Locate every blood parasite and identify its species.
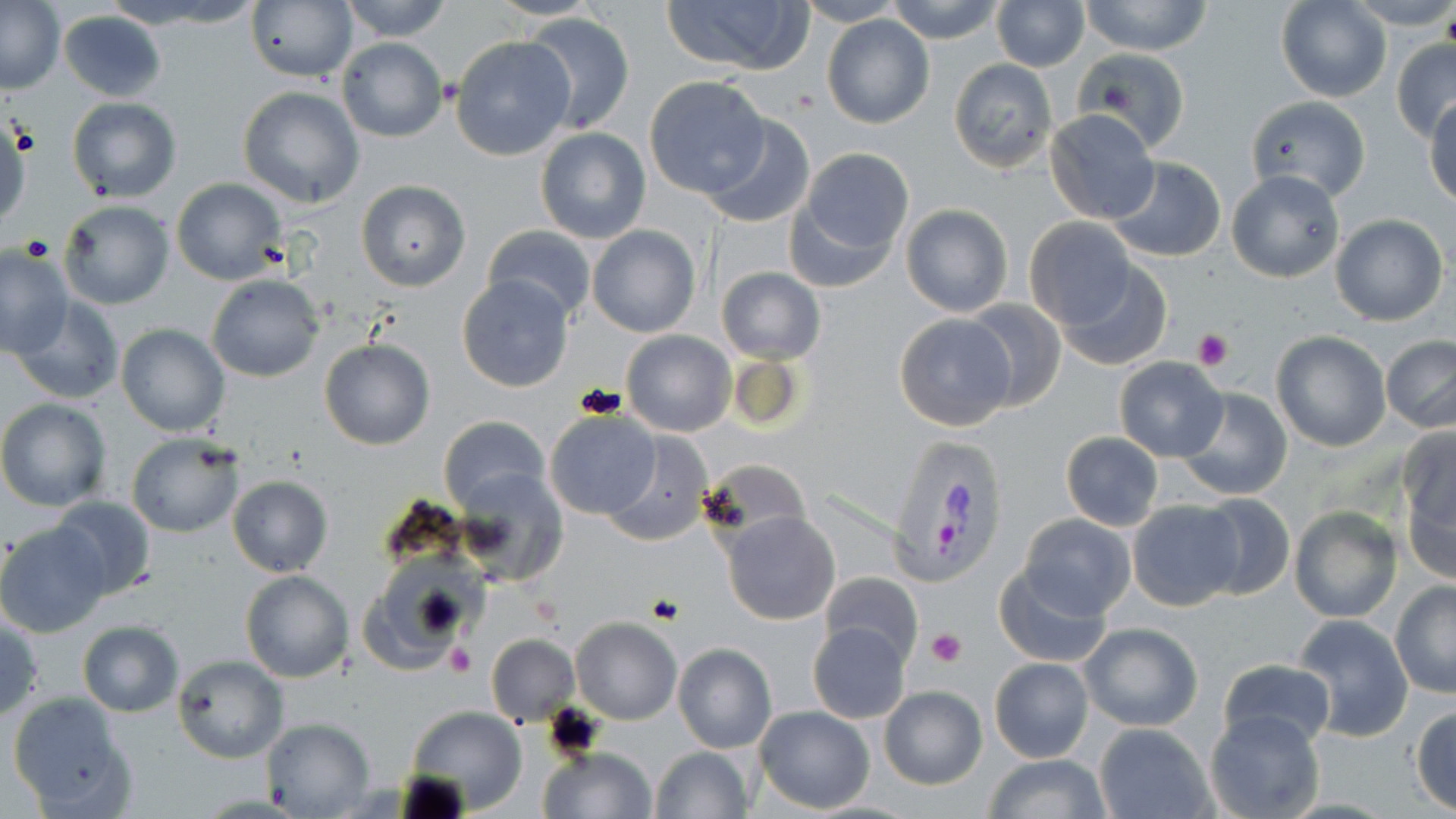

Approximate bounding boxes as [x1, y1, x2, y2] in pixels.
Plasmodium vivax-infected red blood cells: [884, 433, 1009, 587].
No Plasmodium falciparum, Plasmodium ovale, Plasmodium malariae, Babesia divergens, or Trypanosoma brucei observed.

Summary:
  - Platelet locations: [1194, 330, 1234, 368], [927, 628, 967, 668], [444, 641, 475, 675]
  - Uninfected red blood cell locations: [102, 0, 250, 30], [338, 0, 454, 41], [660, 0, 813, 77], [794, 0, 906, 27], [885, 0, 1006, 44], [992, 0, 1088, 71], [1079, 0, 1215, 55], [1347, 0, 1456, 31], [1, 1, 64, 94], [1274, 1, 1392, 103], [246, 2, 356, 82], [59, 10, 167, 104], [521, 11, 635, 135], [822, 14, 935, 129], [450, 35, 576, 161], [335, 36, 447, 143], [1391, 37, 1456, 141], [1072, 48, 1189, 152], [949, 58, 1058, 173], [643, 75, 768, 196], [236, 86, 365, 208], [1245, 96, 1371, 204], [66, 97, 182, 202], [1425, 101, 1456, 207], [1043, 109, 1160, 225], [0, 112, 32, 233], [698, 115, 816, 229], [535, 126, 650, 242], [790, 149, 914, 274], [1106, 156, 1227, 263], [1227, 169, 1343, 282], [171, 177, 288, 285], [356, 180, 471, 291], [61, 191, 287, 298], [59, 199, 175, 310], [899, 204, 1014, 317], [1330, 213, 1448, 326], [1024, 217, 1136, 326], [587, 224, 700, 339], [482, 225, 597, 322], [0, 245, 74, 358], [1057, 259, 1172, 371], [717, 267, 824, 363], [456, 273, 575, 392], [207, 274, 324, 382], [11, 295, 126, 406], [964, 299, 1065, 412], [892, 312, 1019, 432], [116, 324, 230, 437], [621, 329, 736, 436], [1271, 331, 1391, 452], [1380, 335, 1456, 433], [319, 338, 434, 450], [1113, 356, 1228, 461], [1174, 387, 1294, 501], [0, 399, 113, 511], [544, 410, 659, 520], [439, 416, 550, 512], [1396, 427, 1456, 551], [603, 432, 713, 547], [1060, 432, 1164, 530], [126, 433, 246, 538], [697, 459, 808, 542], [458, 467, 569, 588], [227, 474, 332, 577], [1193, 493, 1294, 601], [48, 495, 157, 600], [1126, 499, 1242, 611], [1289, 505, 1401, 623], [721, 512, 840, 626], [1018, 512, 1137, 620], [0, 521, 110, 636], [365, 557, 477, 669], [992, 565, 1114, 668], [241, 570, 353, 683], [819, 572, 923, 671], [1390, 580, 1456, 698], [1292, 614, 1414, 741], [1, 615, 43, 722], [571, 617, 682, 724], [76, 620, 184, 716], [808, 622, 911, 723], [1079, 622, 1203, 732], [570, 629, 777, 737], [485, 635, 579, 726], [672, 643, 777, 753], [172, 654, 287, 762], [989, 658, 1094, 763], [1217, 659, 1337, 752], [878, 685, 986, 789], [6, 692, 133, 815], [1410, 704, 1456, 814], [404, 705, 526, 813], [754, 706, 874, 813], [1204, 709, 1326, 819], [261, 717, 376, 817], [1093, 722, 1215, 818], [537, 746, 656, 818], [648, 747, 753, 819], [982, 755, 1114, 817]
  - Slide-level diagnosis: Plasmodium vivax
  - Image size: 1456×819 pixels
  - Modality: light microscopy
  - Field of view: single
  - Stain: May-Grünwald-Giemsa
  - Magnification: 1000x
  - Preparation: thin blood film